Report the malaria status of this cell.
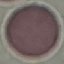

It is uninfected.

image type = automatically extracted cell patch, resized to 64 × 64 pixels
capture = smartphone through the microscope eyepiece
stain = Giemsa
preparation = thin smear